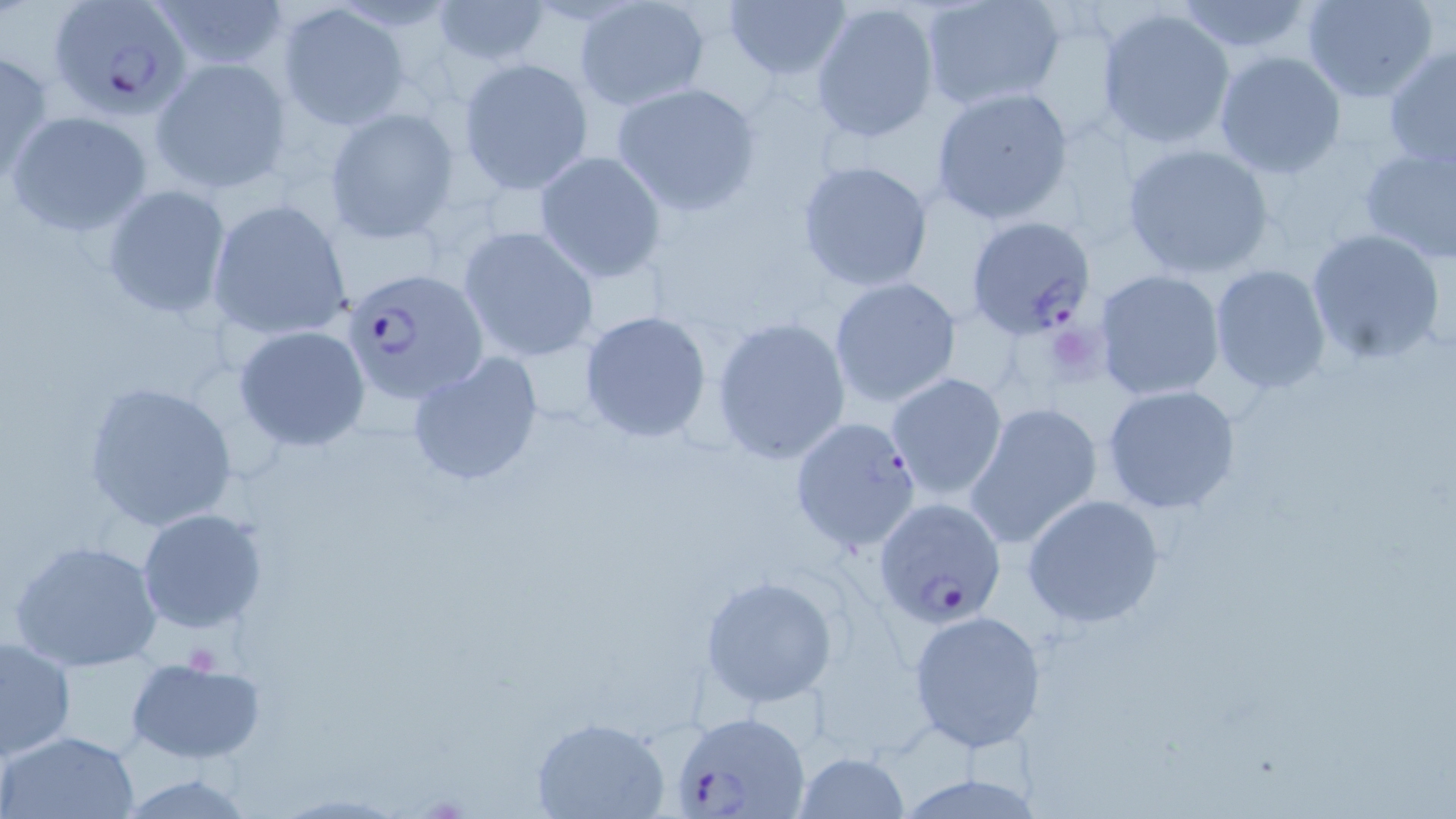
Approximate bounding boxes as [x1, y1, x2, y2] in pixels. Plasmodium falciparum-infected red blood cell locations: [47, 1, 195, 119], [966, 216, 1096, 339], [341, 266, 487, 405], [790, 417, 922, 554], [872, 497, 1008, 628], [672, 715, 811, 819]. Uninfected red blood cell locations: [723, 0, 852, 83], [1301, 0, 1440, 103], [428, 1, 554, 68], [808, 1, 943, 145], [1172, 1, 1319, 56], [573, 2, 709, 112], [922, 2, 1068, 113], [278, 5, 409, 129], [1095, 6, 1235, 150], [1382, 45, 1456, 170], [0, 48, 51, 184], [1213, 50, 1347, 178], [151, 56, 293, 195], [459, 57, 593, 195], [609, 81, 763, 218], [930, 85, 1075, 226], [323, 106, 460, 243], [6, 110, 153, 237], [1356, 141, 1456, 267], [1122, 143, 1276, 279], [534, 150, 668, 284], [794, 159, 934, 291], [100, 185, 233, 320], [208, 199, 353, 344], [457, 227, 601, 362], [1304, 227, 1446, 365], [1207, 263, 1331, 396], [1093, 269, 1226, 401], [828, 275, 962, 408], [577, 309, 714, 444], [712, 316, 851, 465], [232, 325, 371, 452], [406, 351, 545, 488], [885, 371, 1008, 503], [83, 379, 238, 532], [1100, 383, 1243, 516], [964, 402, 1103, 550], [1021, 493, 1167, 629], [136, 508, 270, 635], [8, 538, 165, 673], [700, 574, 840, 709], [907, 609, 1046, 753], [1, 633, 77, 761], [124, 656, 268, 764], [531, 717, 670, 819], [3, 730, 140, 818], [793, 751, 910, 819], [895, 772, 1045, 817]. Slide-level diagnosis: Plasmodium falciparum. Thin blood film. May-Grünwald-Giemsa-stained preparation. Single field of view. Captured at 1000x magnification. Optical microscopy. Image is 1456×819 pixels.